Classify this cell by malaria status.
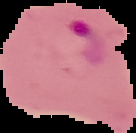

It is parasitized.

image type = segmented cell region on a black background
image size = 136×133 pixels
preparation = thin blood smear